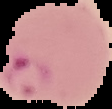
image_size: 112×109 pixels
image_type: segmented cell region with the area outside set to black
malaria_status: parasitized
preparation: thin blood film